Describe the morphology of the erythrocytes.
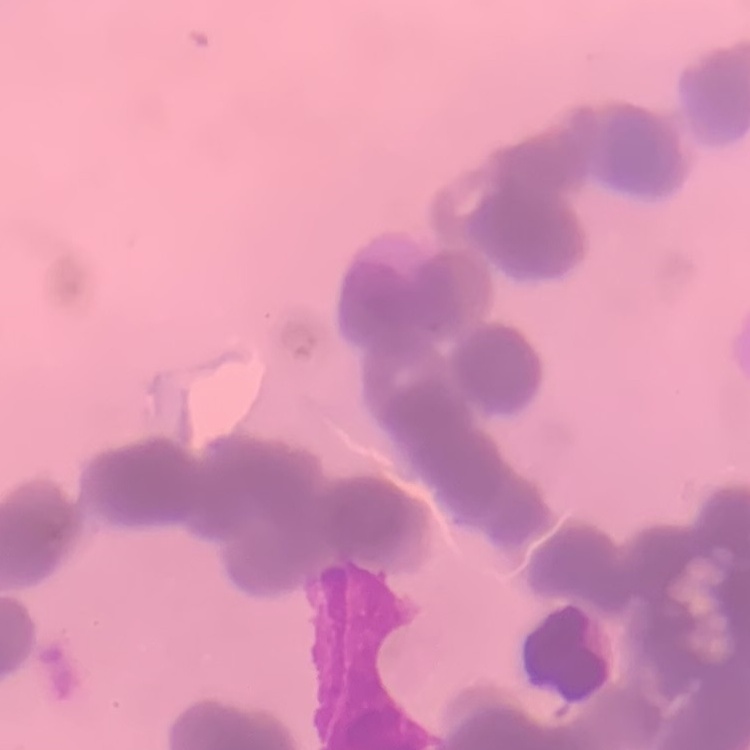

They show rouleaux formation.

Field's or Giemsa stain. One tile cut from a larger photomicrograph. Thin peripheral smear.